Assess this cell for malaria.
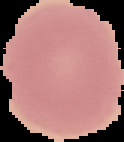
It is uninfected.

Summary:
  - Preparation: thin blood smear
  - Image type: segmented cell region on a black background
  - Image size: 124×142 pixels